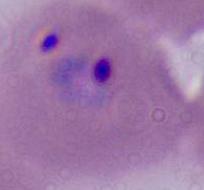

identification = Plasmodium
modality = micrograph
magnification = 400x or 1000x